State which cell type is depicted.
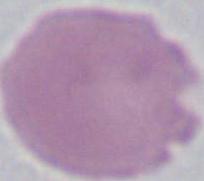

This is an erythrocyte.

Micrograph. 1000x magnification.